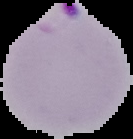

From a thin blood smear. Result: malaria parasites detected. Cell region segmented out of the field of view; the surrounding area is masked to black. Image is 133×139 pixels.